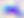
modality: photomicrograph
identification: Toxoplasma gondii
magnification: 400x